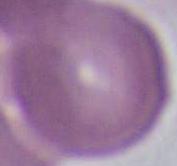
Summary:
  - Magnification: 1000x
  - Identification: erythrocyte
  - Modality: micrograph